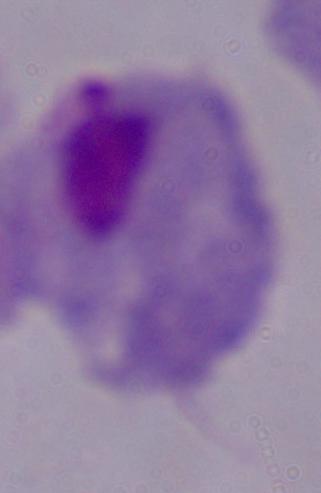

Summary:
  - Modality: photomicrograph
  - Identification: trichomonad
  - Magnification: 1000x